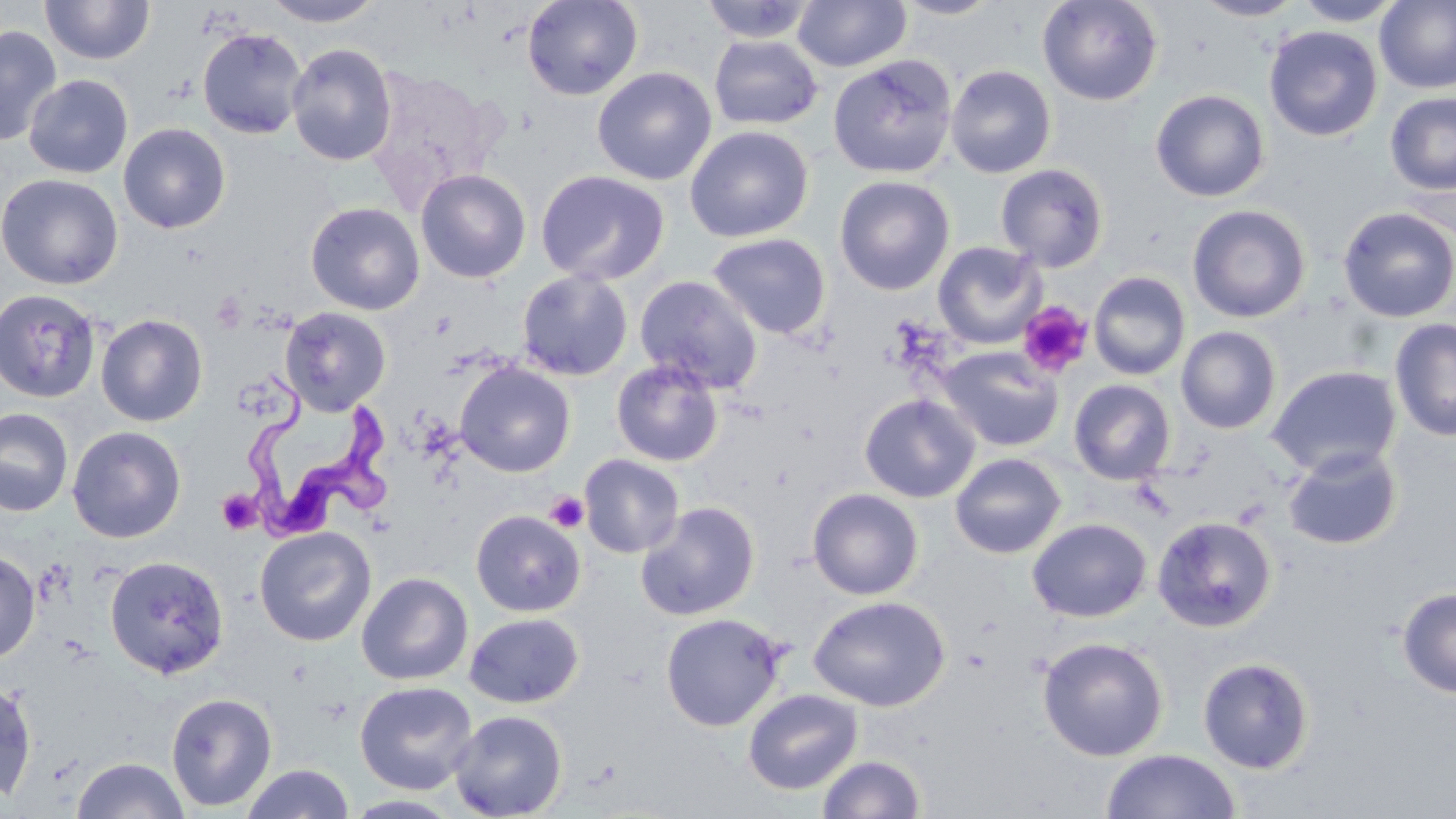

slide_level_diagnosis: Trypanosoma brucei
field_of_view: single
trypanosoma_brucei_locations: 'approximate bounding boxes as (x1, y1, x2, y2) in pixels: (245, 369, 398, 542)'
magnification: 1000x
image_size: 1456×819 pixels
modality: light microscopy
stain: May-Grünwald-Giemsa
uninfected_red_blood_cell_locations: 'approximate bounding boxes as (x1, y1, x2, y2) in pixels: (262, 0, 386, 27), (522, 0, 643, 100), (699, 0, 818, 43), (793, 0, 911, 72), (894, 0, 1004, 19), (1036, 0, 1163, 106), (1191, 0, 1306, 21), (1292, 0, 1405, 26), (40, 1, 155, 65), (1375, 1, 1456, 94), (0, 25, 61, 147), (1264, 25, 1382, 141), (197, 28, 307, 139), (709, 35, 824, 130), (287, 44, 397, 166), (827, 56, 958, 179), (945, 65, 1056, 178), (365, 66, 502, 208), (592, 66, 717, 186), (24, 75, 133, 178), (1150, 89, 1270, 202), (1385, 91, 1456, 195), (118, 123, 231, 233), (685, 125, 813, 243), (995, 163, 1108, 271), (416, 169, 531, 283), (536, 170, 670, 286), (0, 173, 123, 290), (834, 175, 955, 296), (305, 201, 425, 315), (1187, 204, 1311, 323), (1337, 206, 1456, 323), (707, 233, 831, 340), (933, 241, 1046, 349), (517, 270, 633, 381), (1088, 271, 1191, 380), (634, 275, 763, 394), (0, 289, 102, 403), (279, 307, 391, 415), (96, 314, 208, 427), (1389, 317, 1456, 442), (1176, 326, 1281, 434), (935, 346, 1065, 452), (611, 360, 723, 466), (454, 362, 576, 477), (1266, 365, 1401, 479), (1069, 379, 1176, 485), (859, 393, 980, 503), (0, 407, 74, 517), (67, 425, 186, 543), (1283, 446, 1402, 550), (950, 453, 1066, 559), (579, 454, 684, 558), (807, 488, 924, 600), (636, 501, 760, 621), (471, 510, 585, 617), (1151, 515, 1277, 633), (1027, 518, 1152, 622), (255, 526, 376, 646), (0, 550, 40, 664), (104, 555, 229, 679), (357, 572, 473, 685), (1396, 586, 1456, 699), (807, 595, 950, 710), (660, 612, 786, 731), (464, 613, 583, 708), (1037, 636, 1169, 761), (1197, 656, 1315, 774), (0, 677, 38, 804), (355, 681, 478, 794), (743, 688, 863, 795), (165, 692, 278, 811), (449, 710, 567, 819), (1100, 749, 1241, 819), (817, 754, 926, 818), (72, 757, 188, 819), (241, 764, 355, 819), (343, 794, 464, 818)'
platelet_locations: 'approximate bounding boxes as (x1, y1, x2, y2) in pixels: (1018, 301, 1093, 379), (217, 489, 262, 534), (544, 491, 588, 532)'
preparation: thin blood film